Locate every blood parasite and identify its species.
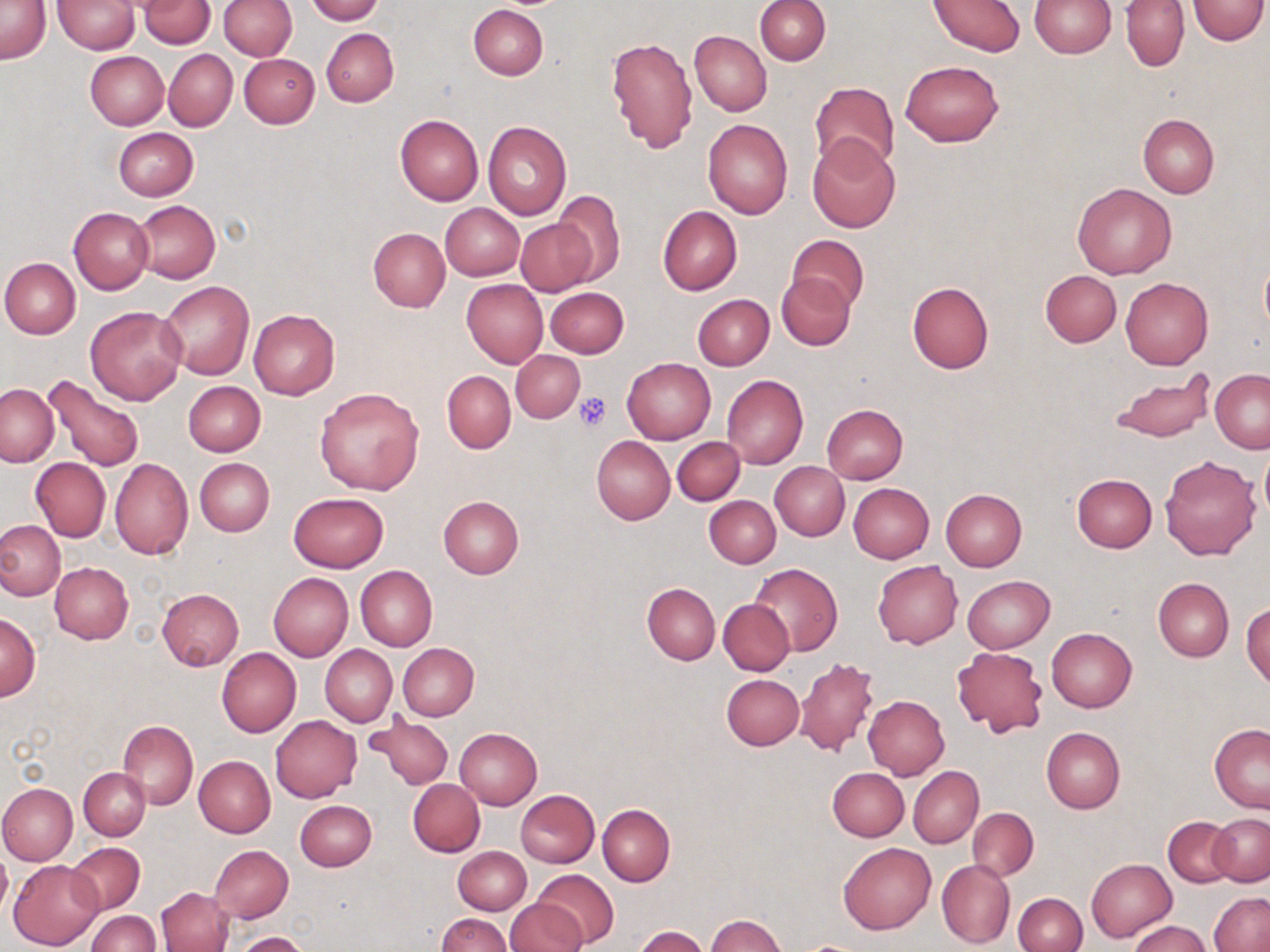

No blood parasites observed.

Approximate bounding boxes as [x1, y1, x2, y2] in pixels. Platelet locations: [574, 392, 610, 431]. Uninfected red blood cell locations: [53, 0, 140, 54], [137, 0, 217, 48], [218, 0, 297, 60], [306, 0, 383, 23], [717, 0, 811, 78], [755, 0, 830, 65], [928, 0, 1026, 56], [1029, 0, 1115, 57], [1122, 0, 1189, 71], [1186, 0, 1268, 44], [1, 1, 50, 64], [227, 1, 303, 125], [468, 5, 548, 80], [322, 28, 398, 106], [690, 31, 772, 116], [606, 36, 698, 153], [164, 49, 237, 131], [85, 52, 169, 129], [239, 53, 319, 128], [901, 60, 1004, 147], [810, 81, 899, 175], [1138, 113, 1219, 197], [394, 114, 484, 205], [703, 119, 793, 219], [483, 121, 572, 220], [113, 128, 198, 201], [807, 136, 902, 234], [1073, 182, 1176, 279], [552, 191, 625, 285], [133, 200, 219, 284], [439, 203, 524, 280], [658, 206, 742, 295], [69, 207, 153, 294], [515, 217, 597, 295], [368, 227, 450, 312], [787, 234, 868, 311], [1, 257, 81, 339], [1040, 270, 1122, 347], [777, 273, 856, 350], [1120, 277, 1213, 369], [461, 279, 548, 367], [160, 280, 254, 380], [906, 282, 994, 374], [545, 286, 628, 357], [693, 293, 774, 371], [85, 305, 188, 405], [248, 309, 339, 399], [511, 349, 585, 421], [622, 358, 715, 444], [1210, 368, 1270, 453], [1109, 370, 1215, 441], [442, 371, 515, 453], [42, 374, 144, 474], [722, 374, 808, 469], [183, 381, 266, 456], [1, 384, 58, 467], [314, 387, 426, 494], [821, 403, 907, 485], [590, 436, 674, 525], [673, 438, 744, 506], [1258, 446, 1269, 522], [1160, 455, 1261, 559], [194, 457, 274, 536], [30, 458, 111, 540], [110, 458, 193, 561], [770, 462, 849, 540], [1071, 473, 1157, 553], [848, 483, 934, 563], [940, 489, 1027, 571], [287, 492, 389, 573], [437, 495, 524, 578], [704, 496, 781, 567], [0, 520, 64, 600], [873, 561, 963, 649], [50, 562, 133, 643], [750, 563, 842, 656], [355, 565, 437, 652], [268, 572, 353, 662], [963, 575, 1055, 653], [1154, 577, 1234, 662], [642, 583, 719, 664], [156, 589, 243, 670], [718, 598, 794, 676], [1242, 602, 1270, 687], [1, 613, 40, 700], [1046, 628, 1136, 712], [398, 643, 479, 720], [320, 645, 397, 727], [951, 647, 1047, 738], [216, 648, 301, 737], [794, 658, 880, 757], [722, 674, 804, 749], [863, 695, 950, 779], [366, 713, 455, 791], [270, 715, 362, 802], [118, 719, 197, 809], [1209, 724, 1270, 812], [455, 727, 542, 809], [1041, 727, 1125, 812], [194, 756, 275, 837], [909, 766, 983, 848], [78, 767, 150, 840], [828, 768, 909, 841], [408, 779, 485, 856], [0, 782, 77, 865], [515, 789, 599, 866], [296, 800, 377, 872], [598, 805, 675, 886], [967, 808, 1038, 882], [1209, 812, 1269, 886], [1163, 816, 1238, 888], [838, 842, 935, 933], [68, 843, 145, 916], [209, 846, 293, 922], [453, 846, 531, 915], [0, 848, 11, 921], [936, 858, 1016, 949], [1086, 858, 1176, 943], [9, 859, 104, 949], [530, 868, 618, 948], [1009, 886, 1158, 952], [157, 887, 234, 952], [1014, 892, 1087, 952], [1209, 892, 1270, 952], [505, 900, 586, 952], [88, 911, 159, 952], [438, 913, 511, 952], [706, 914, 787, 952], [1129, 920, 1212, 952], [633, 926, 709, 952], [234, 932, 313, 952]. Slide-level diagnosis: negative for blood parasites. Optical microscopy. Image is 1270×952 pixels. Captured at 1000x magnification. Thin blood smear. May-Grünwald-Giemsa stain. Single field of view.